Report the malaria status of this cell.
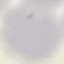

It is uninfected.

preparation: thin blood film
stain: Giemsa
capture: smartphone camera at the microscope eyepiece
image_type: automatically extracted cell patch, resized to 64 × 64 pixels